State which parasite is depicted.
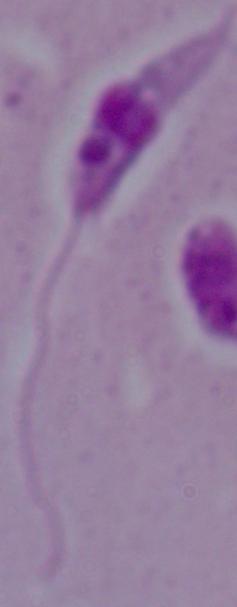
This is Leishmania.

1000x magnification. Micrograph.